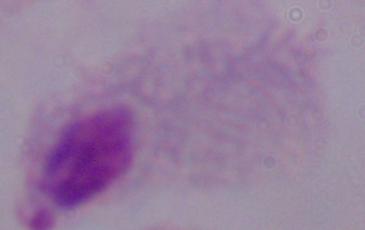
identification: trichomonad
modality: micrograph
magnification: 1000x